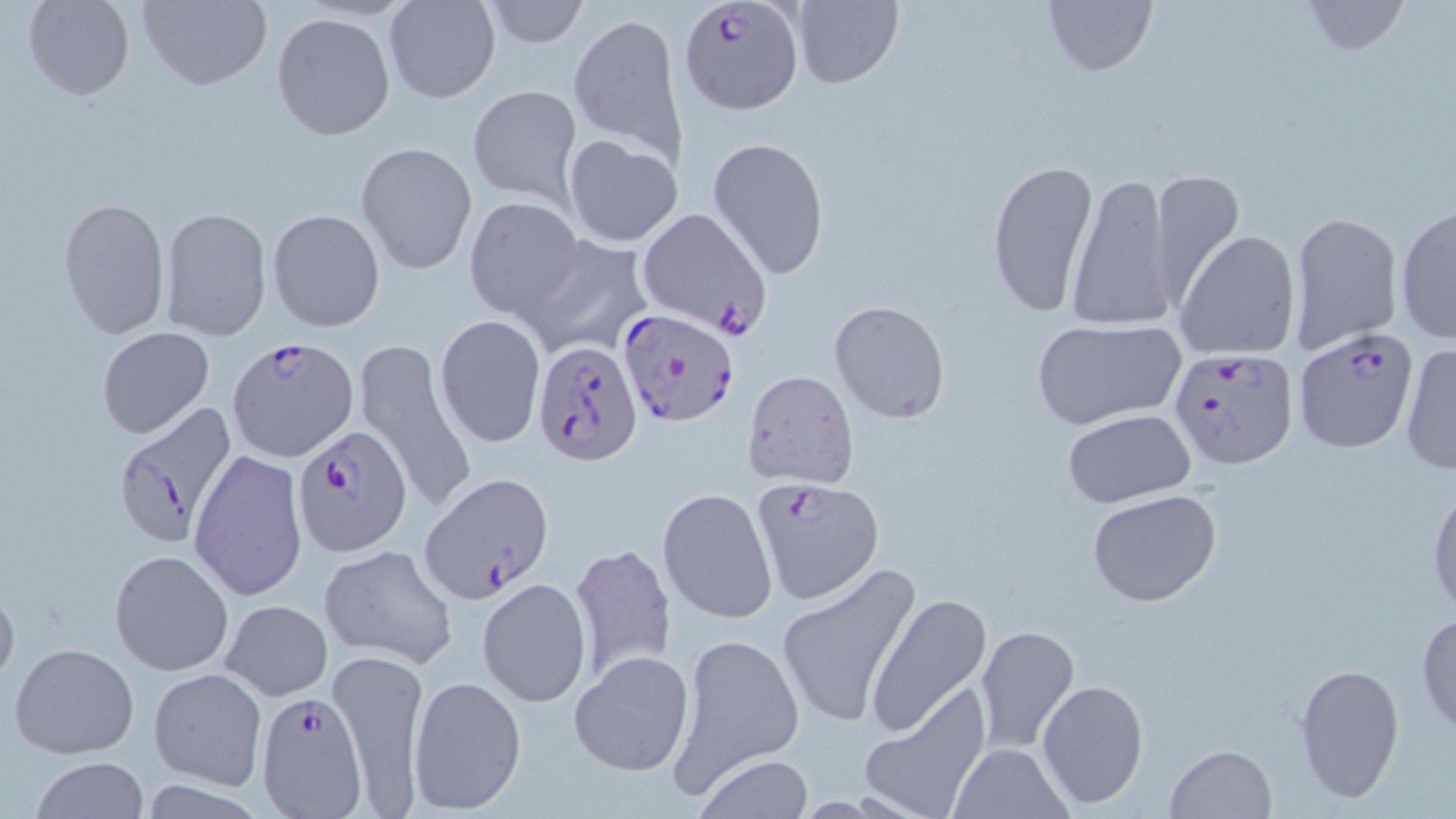

Approximate bounding boxes as (x1,y1)-(x2,y2) corner pairs in pixels. Plasmodium falciparum-infected red blood cell locations: (678,1)-(804,116), (614,307)-(739,427), (1291,328)-(1420,454), (227,336)-(359,463), (529,337)-(643,463), (1167,346)-(1300,470), (111,402)-(239,549), (293,424)-(410,557), (420,472)-(553,602), (750,476)-(883,606), (257,690)-(369,818). Uninfected red blood cell locations: (23,0)-(134,100), (137,0)-(271,90), (382,0)-(501,104), (479,0)-(590,49), (1041,0)-(1157,78), (791,1)-(903,90), (1299,1)-(1410,56), (568,11)-(684,160), (271,12)-(395,141), (467,84)-(581,206), (564,136)-(683,248), (707,136)-(830,280), (354,142)-(476,274), (986,157)-(1099,318), (1149,171)-(1241,308), (1066,174)-(1177,331), (463,195)-(582,319), (57,196)-(171,340), (1396,206)-(1456,343), (635,207)-(773,338), (160,208)-(272,340), (267,208)-(386,332), (1286,210)-(1402,354), (1175,231)-(1301,361), (518,234)-(654,358), (830,301)-(949,424), (434,314)-(547,449), (1030,319)-(1185,430), (97,327)-(214,438), (354,342)-(476,514), (1399,342)-(1456,477), (741,369)-(859,489), (1063,410)-(1198,510), (189,450)-(307,603), (1427,481)-(1456,621), (657,486)-(778,624), (1086,487)-(1223,607), (570,541)-(676,683), (319,544)-(458,668), (110,550)-(235,675), (774,564)-(921,732), (477,578)-(591,708), (0,582)-(20,693), (867,592)-(992,735), (220,599)-(332,701), (1415,611)-(1456,735), (973,625)-(1080,753), (670,631)-(803,792), (9,642)-(139,759), (328,649)-(429,811), (569,650)-(696,778), (1293,661)-(1405,805), (149,668)-(267,788), (408,674)-(527,816), (1037,677)-(1149,810), (859,686)-(992,818), (946,742)-(1072,818), (1163,744)-(1276,819), (28,756)-(150,818), (693,757)-(817,817). Slide-level diagnosis: Plasmodium falciparum. Single field of view. Optical microscopy. 1000x magnification. Image is 1456×819 pixels. Thin blood smear. May-Grünwald-Giemsa-stained preparation.